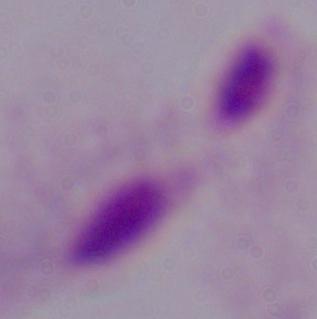
A trichomonad is seen. Photomicrograph. 1000x magnification.